Locate and identify every blood parasite.
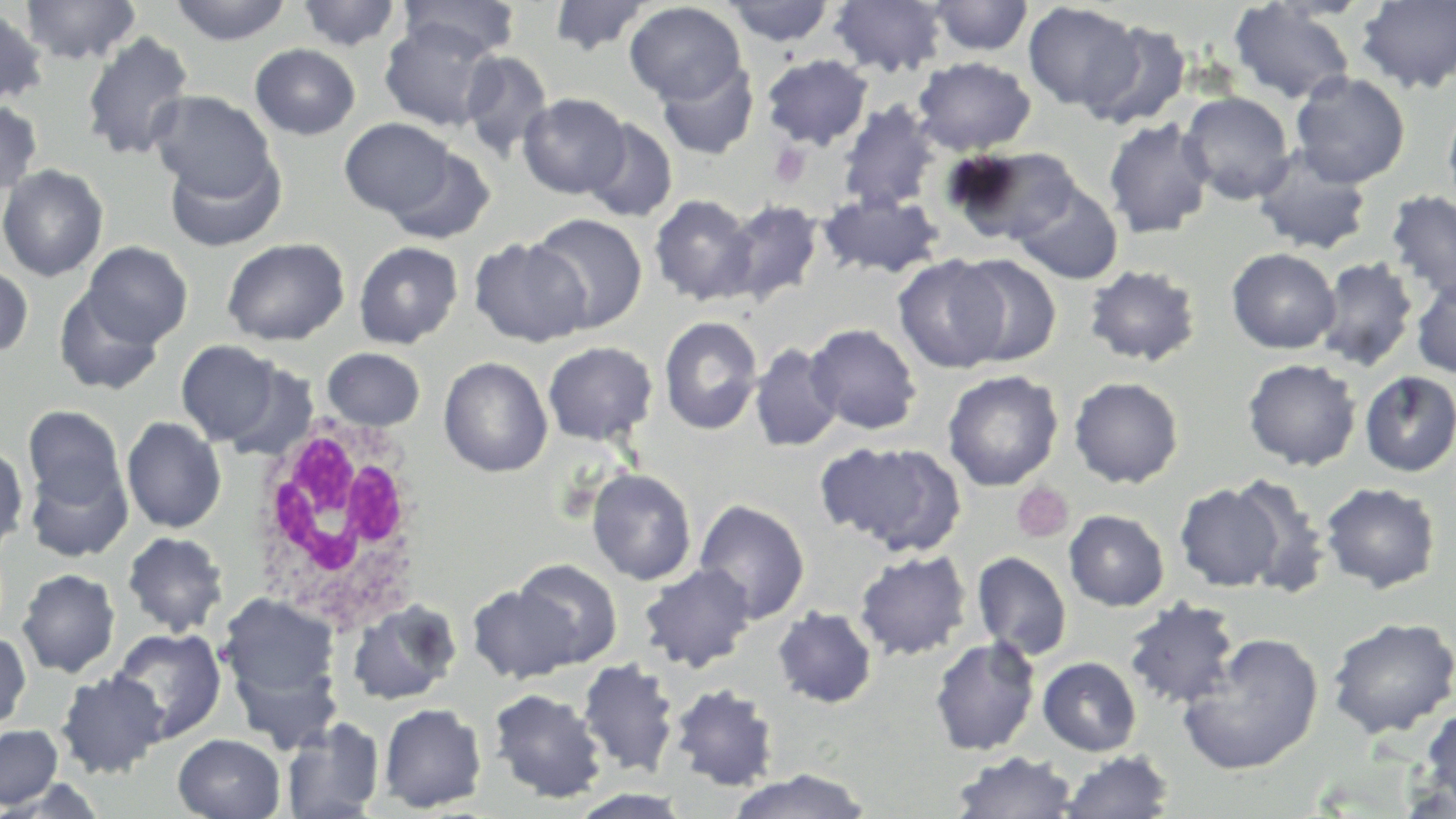
No blood parasites seen.

Summary:
  - Coordinate format: approximate bounding boxes as (x1,y1)-(x2,y2) corner pairs in pixels
  - White blood cell locations: (245,412)-(425,630)
  - Uninfected red blood cell locations: (21,0)-(141,66), (170,0)-(293,46), (398,0)-(521,60), (548,0)-(650,56), (722,0)-(836,47), (828,0)-(948,78), (926,0)-(1034,57), (296,1)-(403,52), (1229,1)-(1356,105), (1355,1)-(1456,93), (625,2)-(746,105), (1022,2)-(1141,112), (0,8)-(48,107), (380,19)-(501,131), (1084,21)-(1191,130), (81,31)-(195,161), (250,44)-(360,140), (460,51)-(554,161), (761,54)-(873,150), (912,56)-(1036,155), (656,60)-(759,160), (1290,71)-(1411,188), (149,90)-(276,199), (1179,91)-(1295,205), (518,93)-(630,199), (0,99)-(42,196), (1442,100)-(1456,214), (837,101)-(940,213), (1103,117)-(1214,239), (340,118)-(456,219), (582,118)-(677,223), (383,145)-(494,244), (945,145)-(1080,245), (164,147)-(286,252), (1252,147)-(1373,256), (0,164)-(108,281), (1011,181)-(1123,285), (1386,190)-(1456,303), (819,192)-(944,279), (649,194)-(759,306), (721,199)-(823,305), (526,213)-(648,333), (468,236)-(592,347), (222,237)-(350,346), (82,241)-(192,346), (353,241)-(462,349), (1226,248)-(1340,354), (953,254)-(1061,366), (893,255)-(1009,373), (1315,256)-(1419,372), (0,264)-(33,357), (1084,264)-(1201,367), (1080,265)-(1194,486), (1411,273)-(1456,379), (54,287)-(164,396), (659,315)-(764,435), (805,323)-(922,435), (176,340)-(282,446), (542,341)-(658,446), (750,343)-(843,452), (321,347)-(426,431), (439,356)-(553,477), (1242,358)-(1361,470), (222,362)-(318,463), (942,370)-(1064,491), (1358,370)-(1456,477), (1068,377)-(1183,488), (23,405)-(125,509), (122,416)-(226,533), (816,441)-(964,554), (0,443)-(28,557), (26,459)-(133,563), (586,467)-(697,585), (1227,475)-(1330,598), (1174,482)-(1286,591), (1320,482)-(1441,594), (693,499)-(810,623), (1064,510)-(1169,611), (122,531)-(229,637), (854,550)-(972,660), (971,551)-(1072,660), (513,558)-(622,666), (639,562)-(757,673), (17,568)-(120,678), (466,583)-(582,684), (218,592)-(342,713), (1123,598)-(1240,709), (346,599)-(462,706), (772,606)-(878,709), (1325,616)-(1455,739), (109,627)-(227,743), (0,631)-(31,734), (1177,633)-(1324,775), (928,636)-(1042,756), (228,649)-(344,756), (1037,656)-(1142,756), (577,659)-(679,777), (54,670)-(168,778), (670,684)-(778,791), (488,688)-(608,804), (379,703)-(487,813), (1419,706)-(1456,815), (281,717)-(385,819), (0,724)-(63,810), (173,734)-(285,819), (1059,750)-(1174,818), (950,751)-(1078,818), (725,768)-(872,819)
  - Platelet locations: (769,143)-(811,187), (1012,483)-(1073,544)
  - Slide-level diagnosis: negative for blood parasites
  - Preparation: thin blood smear
  - Stain: May-Grünwald-Giemsa
  - Field of view: one of a larger specimen
  - Modality: optical microscopy
  - Image size: 1456×819 pixels
  - Magnification: 1000x